Identify the parasite.
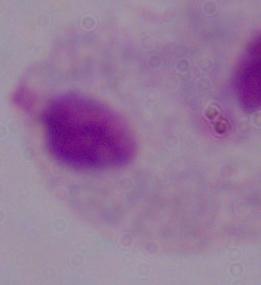

This is a trichomonad.

Micrograph. 1000x magnification.